Name the blood parasite species.
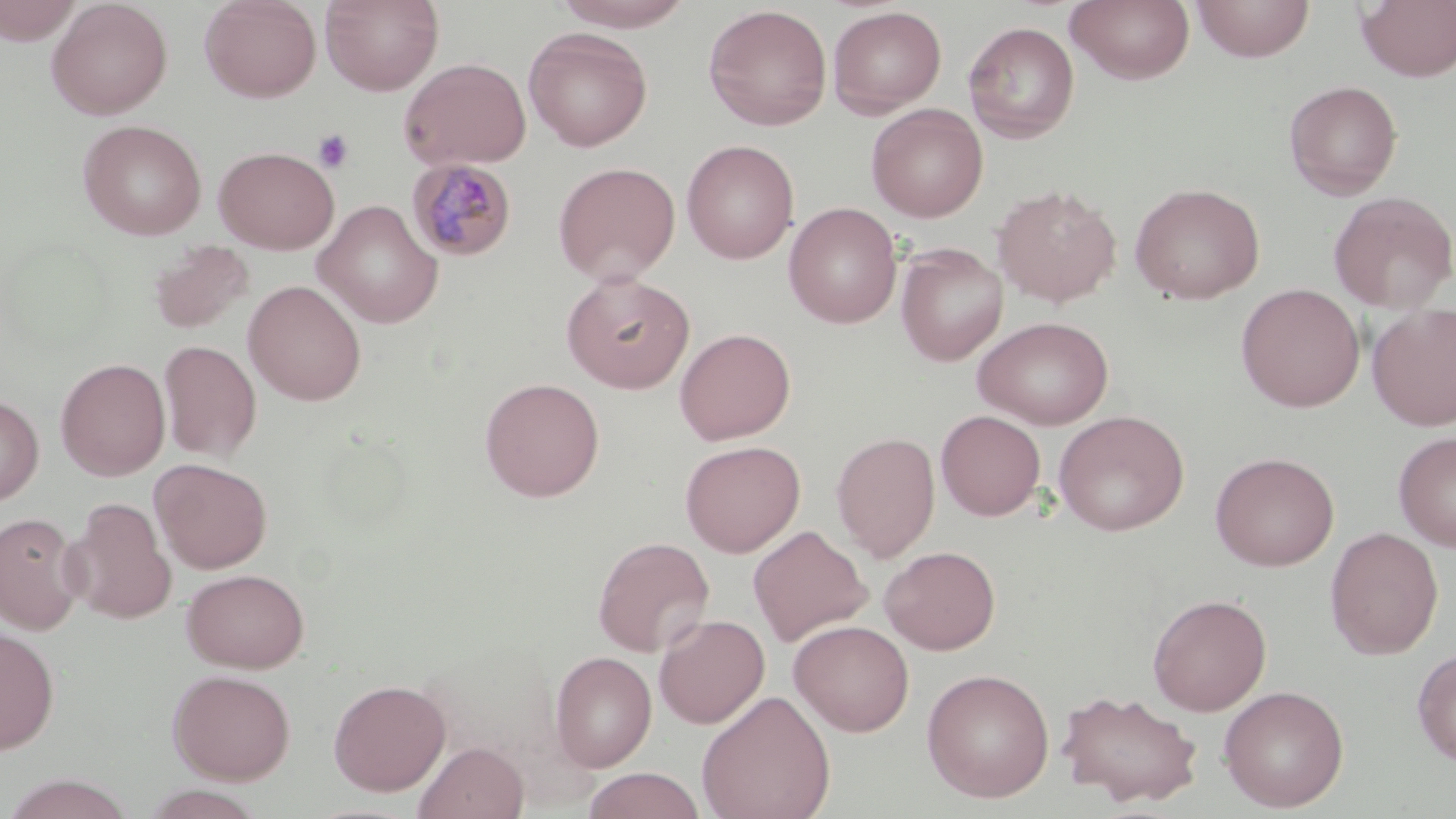

Plasmodium malariae.

Approximate bounding boxes as (x1, y1, x2, y2) in pixels. Platelet locations: (312, 128, 354, 174). Plasmodium malariae-infected red blood cell locations: (406, 158, 517, 262). Uninfected red blood cell locations: (46, 0, 173, 120), (199, 0, 321, 102), (320, 0, 444, 96), (550, 0, 694, 30), (1066, 0, 1196, 85), (1192, 0, 1314, 62), (1355, 0, 1456, 82), (1, 1, 83, 44), (703, 4, 832, 131), (828, 6, 947, 117), (964, 21, 1080, 142), (524, 27, 652, 151), (399, 57, 532, 171), (1283, 80, 1402, 200), (866, 103, 988, 222), (77, 119, 207, 240), (681, 139, 799, 264), (213, 145, 339, 254), (553, 161, 680, 285), (1129, 182, 1266, 304), (992, 185, 1122, 307), (1328, 191, 1456, 313), (313, 199, 444, 328), (784, 202, 902, 329), (148, 240, 254, 335), (896, 243, 1008, 365), (562, 272, 695, 394), (244, 280, 366, 406), (1236, 283, 1365, 412), (1368, 303, 1456, 431), (974, 316, 1113, 429), (674, 327, 796, 445), (159, 340, 261, 462), (56, 358, 170, 481), (479, 377, 604, 502), (0, 394, 44, 506), (936, 410, 1046, 520), (1053, 410, 1189, 536), (1394, 430, 1456, 554), (831, 431, 940, 561), (680, 440, 805, 557), (1210, 451, 1339, 571), (151, 459, 272, 574), (67, 497, 175, 624), (0, 512, 86, 635), (748, 526, 873, 647), (1325, 526, 1443, 659), (592, 536, 714, 657), (880, 546, 1001, 654), (182, 568, 309, 672), (1147, 593, 1271, 715), (654, 613, 770, 729), (789, 619, 914, 737), (0, 625, 60, 754), (1412, 648, 1456, 766), (550, 650, 657, 772), (920, 667, 1055, 802), (167, 668, 296, 784), (328, 679, 450, 796), (1219, 685, 1349, 812), (1056, 688, 1205, 807), (697, 690, 836, 819), (414, 741, 528, 819), (582, 768, 706, 819), (2, 774, 137, 819). Thin blood smear. May-Grünwald-Giemsa-stained preparation. Single field of view. Optical microscopy. Image is 1456×819 pixels. Captured at 1000x magnification.